Locate and identify every blood parasite.
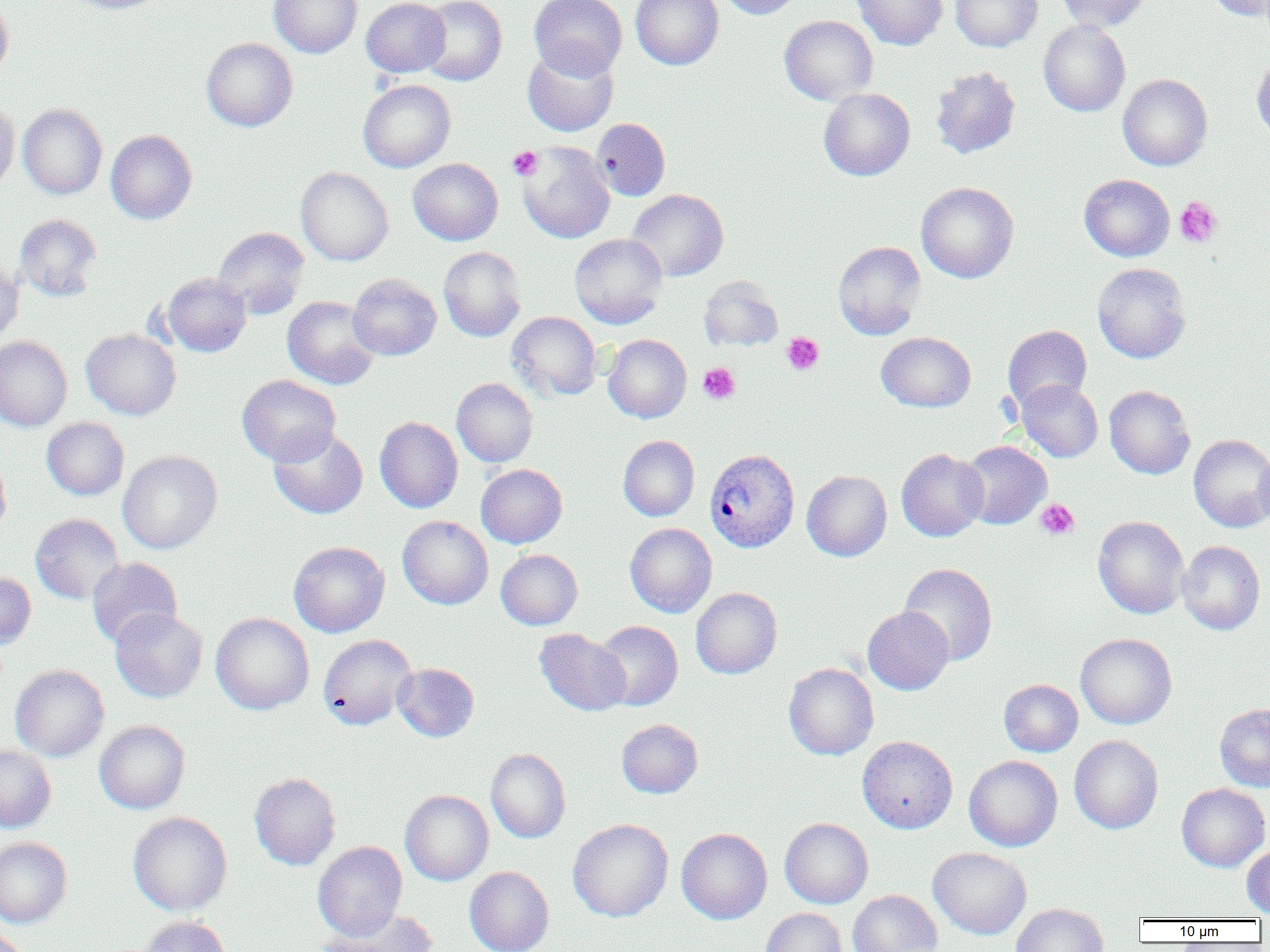
Approximate bounding boxes as named x1/y1/x2/y2 corners in pixels.
Plasmodium vivax-infected red blood cells: (x1=704, y1=448, x2=799, y2=553).
No Plasmodium falciparum, Plasmodium ovale, Plasmodium malariae, Babesia divergens, or Trypanosoma brucei observed.

Uninfected red blood cell locations: (x1=66, y1=0, x2=170, y2=14), (x1=269, y1=0, x2=362, y2=58), (x1=361, y1=0, x2=450, y2=77), (x1=418, y1=0, x2=506, y2=86), (x1=529, y1=0, x2=627, y2=79), (x1=630, y1=0, x2=724, y2=70), (x1=717, y1=0, x2=805, y2=19), (x1=850, y1=0, x2=948, y2=50), (x1=950, y1=0, x2=1043, y2=52), (x1=1054, y1=0, x2=1153, y2=32), (x1=1204, y1=0, x2=1270, y2=21), (x1=0, y1=1, x2=14, y2=84), (x1=779, y1=15, x2=878, y2=105), (x1=1038, y1=19, x2=1130, y2=117), (x1=201, y1=38, x2=297, y2=132), (x1=522, y1=45, x2=618, y2=137), (x1=1251, y1=51, x2=1270, y2=144), (x1=930, y1=66, x2=1020, y2=159), (x1=1118, y1=74, x2=1212, y2=171), (x1=358, y1=79, x2=455, y2=172), (x1=819, y1=88, x2=915, y2=181), (x1=0, y1=100, x2=19, y2=196), (x1=18, y1=104, x2=107, y2=199), (x1=592, y1=117, x2=670, y2=200), (x1=106, y1=130, x2=197, y2=224), (x1=517, y1=141, x2=615, y2=243), (x1=408, y1=158, x2=503, y2=245), (x1=295, y1=166, x2=393, y2=266), (x1=1079, y1=174, x2=1174, y2=261), (x1=916, y1=181, x2=1018, y2=283), (x1=627, y1=189, x2=728, y2=282), (x1=14, y1=213, x2=103, y2=302), (x1=212, y1=227, x2=309, y2=318), (x1=569, y1=233, x2=667, y2=329), (x1=833, y1=241, x2=926, y2=340), (x1=438, y1=246, x2=526, y2=342), (x1=0, y1=256, x2=24, y2=346), (x1=1092, y1=262, x2=1191, y2=363), (x1=161, y1=273, x2=251, y2=357), (x1=347, y1=274, x2=441, y2=361), (x1=698, y1=275, x2=783, y2=351), (x1=282, y1=296, x2=380, y2=390), (x1=507, y1=311, x2=601, y2=401), (x1=1002, y1=325, x2=1092, y2=413), (x1=81, y1=328, x2=181, y2=420), (x1=876, y1=331, x2=975, y2=412), (x1=603, y1=334, x2=691, y2=423), (x1=0, y1=336, x2=72, y2=432), (x1=236, y1=375, x2=341, y2=466), (x1=451, y1=378, x2=538, y2=467), (x1=1016, y1=379, x2=1103, y2=462), (x1=1104, y1=385, x2=1195, y2=479), (x1=375, y1=416, x2=463, y2=513), (x1=41, y1=417, x2=129, y2=500), (x1=268, y1=426, x2=368, y2=519), (x1=1188, y1=434, x2=1270, y2=532), (x1=618, y1=435, x2=700, y2=521), (x1=958, y1=441, x2=1052, y2=530), (x1=1254, y1=444, x2=1270, y2=531), (x1=896, y1=448, x2=988, y2=541), (x1=118, y1=450, x2=222, y2=554), (x1=0, y1=454, x2=11, y2=539), (x1=476, y1=464, x2=567, y2=548), (x1=802, y1=470, x2=892, y2=561), (x1=30, y1=513, x2=124, y2=604), (x1=397, y1=515, x2=493, y2=609), (x1=1093, y1=516, x2=1189, y2=619), (x1=625, y1=523, x2=716, y2=617), (x1=1178, y1=540, x2=1265, y2=634), (x1=289, y1=541, x2=389, y2=637), (x1=495, y1=549, x2=583, y2=630), (x1=86, y1=557, x2=182, y2=647), (x1=899, y1=563, x2=998, y2=665), (x1=0, y1=572, x2=36, y2=648), (x1=691, y1=587, x2=782, y2=679), (x1=863, y1=606, x2=954, y2=695), (x1=109, y1=608, x2=208, y2=702), (x1=211, y1=613, x2=314, y2=715), (x1=594, y1=620, x2=683, y2=711), (x1=534, y1=628, x2=631, y2=716), (x1=1076, y1=633, x2=1176, y2=729), (x1=318, y1=634, x2=416, y2=730), (x1=783, y1=662, x2=879, y2=760), (x1=392, y1=663, x2=479, y2=742), (x1=10, y1=664, x2=109, y2=761), (x1=999, y1=679, x2=1083, y2=757), (x1=1215, y1=704, x2=1270, y2=791), (x1=616, y1=718, x2=703, y2=798), (x1=94, y1=720, x2=190, y2=814), (x1=1069, y1=734, x2=1163, y2=834), (x1=857, y1=735, x2=958, y2=833), (x1=0, y1=744, x2=56, y2=833), (x1=486, y1=748, x2=570, y2=843), (x1=964, y1=755, x2=1062, y2=851), (x1=249, y1=772, x2=341, y2=870), (x1=1176, y1=783, x2=1269, y2=872), (x1=400, y1=790, x2=493, y2=886), (x1=128, y1=812, x2=232, y2=916), (x1=780, y1=817, x2=873, y2=908), (x1=567, y1=818, x2=673, y2=922), (x1=676, y1=828, x2=772, y2=924), (x1=0, y1=837, x2=72, y2=928), (x1=313, y1=841, x2=407, y2=940), (x1=1242, y1=843, x2=1270, y2=917), (x1=928, y1=847, x2=1031, y2=940), (x1=464, y1=866, x2=554, y2=951), (x1=847, y1=890, x2=942, y2=952), (x1=1011, y1=903, x2=1108, y2=952), (x1=761, y1=907, x2=847, y2=952), (x1=320, y1=909, x2=440, y2=952), (x1=140, y1=916, x2=233, y2=952), (x1=0, y1=928, x2=29, y2=952). Platelet locations: (x1=507, y1=146, x2=543, y2=180), (x1=1174, y1=197, x2=1223, y2=248), (x1=782, y1=333, x2=824, y2=375), (x1=698, y1=363, x2=740, y2=404), (x1=1036, y1=499, x2=1079, y2=540). Slide-level diagnosis: Plasmodium vivax. One field of a larger specimen. Image is 1270×952 pixels. Optical microscopy. Thin blood film. Captured at 1000x magnification.